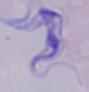

Summary:
  - Magnification: 1000x
  - Modality: micrograph
  - Identification: trypanosome